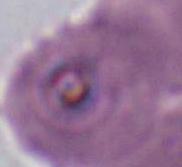

modality = micrograph
magnification = 400x or 1000x
identification = Plasmodium